Assess the morphology of the red blood cells.
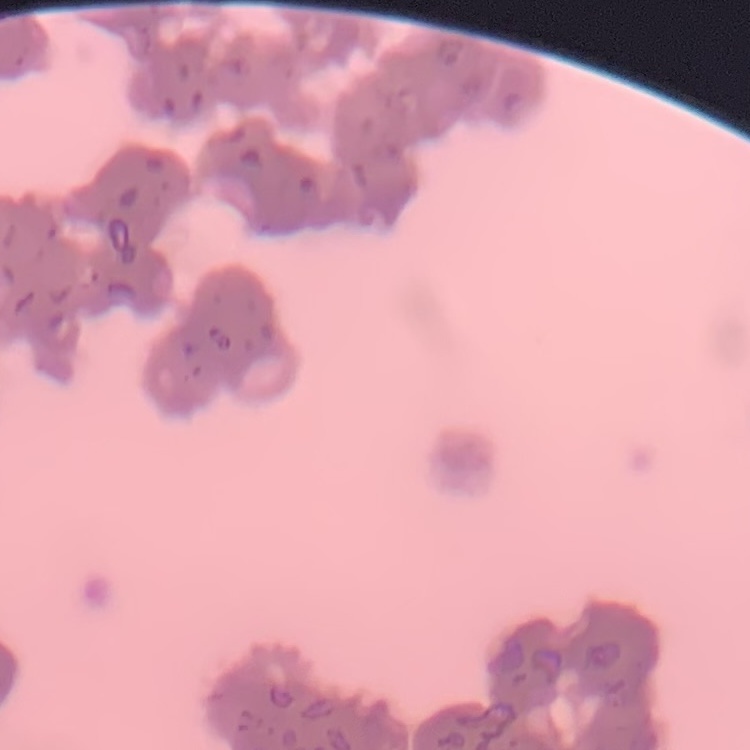
They show rouleaux formation.

image type = square crop of a larger photomicrograph
stain = Field's or Giemsa
preparation = thin peripheral smear